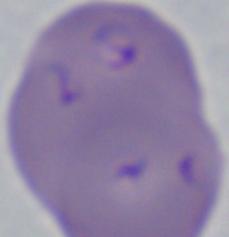

modality = photomicrograph
magnification = 1000x
identification = Babesia